Report the malaria status of this cell.
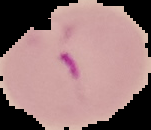
Parasitized.

From a thin blood film. Image is 151×130 pixels. Segmented cell region on a black background.